Report the malaria status of this cell.
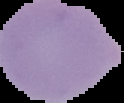

Uninfected.

image type = segmented cell region on a black background
preparation = thin blood smear
image size = 124×103 pixels